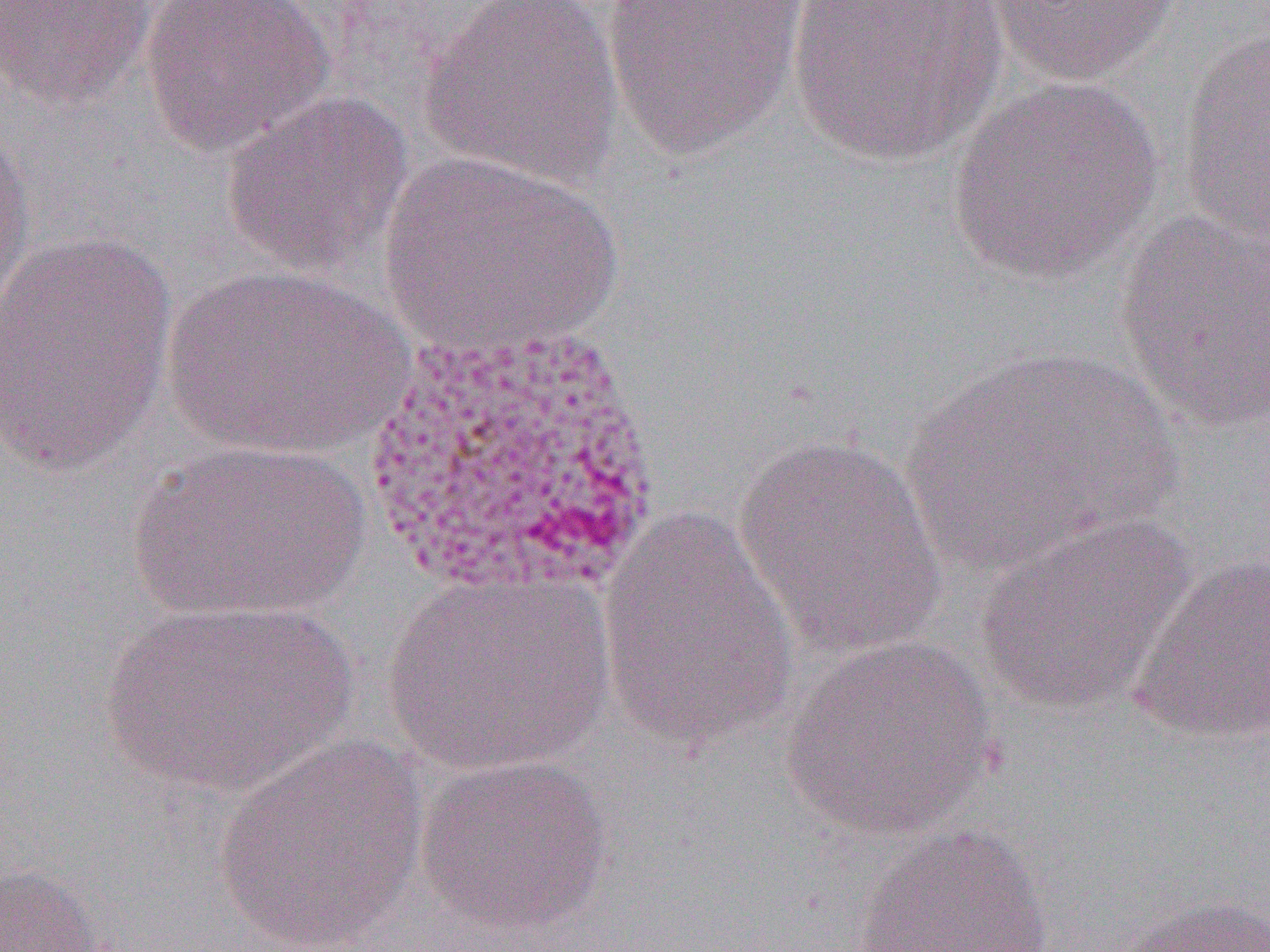

slide_level_diagnosis: Plasmodium vivax
preparation: thin blood smear
uninfected_red_blood_cell_locations: 'approximate bounding boxes as (x1, y1, x2, y2) in pixels: (140, 0, 334, 158), (418, 0, 626, 190), (599, 0, 810, 162), (785, 0, 1008, 167), (984, 0, 1180, 88), (1, 1, 158, 111), (1175, 26, 1270, 253), (948, 76, 1163, 286), (219, 89, 414, 280), (0, 117, 37, 324), (377, 151, 622, 358), (1112, 209, 1269, 437), (0, 230, 180, 482), (161, 265, 415, 461), (898, 345, 1186, 581), (732, 432, 949, 664), (125, 440, 370, 623), (594, 508, 801, 751), (975, 511, 1196, 716), (1129, 550, 1270, 746), (378, 570, 618, 780), (97, 598, 361, 799), (783, 636, 999, 840), (215, 733, 429, 951), (415, 754, 614, 935), (851, 823, 1056, 952), (0, 862, 111, 951), (1114, 893, 1270, 952)'
magnification: 1000x
field_of_view: single
image_size: 1270×952 pixels
modality: optical microscopy